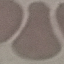

Malaria status: uninfected. Acquired by smartphone through the microscope eyepiece. Cell patch, automatically extracted from a larger field of view and resized to 64 × 64 pixels. Giemsa stain. Thin smear of blood.